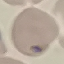

malaria status = uninfected
stain = Giemsa
capture = smartphone camera at the microscope eyepiece
image type = cell patch, automatically extracted from a larger field of view and resized to 64 × 64 pixels
preparation = thin blood film